Assess this cell for malaria.
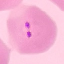
Parasitized.

Cell patch, automatically extracted from a larger field of view and resized to 64 × 64 pixels. Giemsa-stained preparation. Photographed with a smartphone camera at the microscope eyepiece. Thin smear of blood.